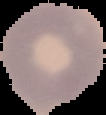
Summary:
  - Image type: segmented cell region on a black background
  - Malaria status: uninfected
  - Preparation: thin blood film
  - Image size: 106×115 pixels